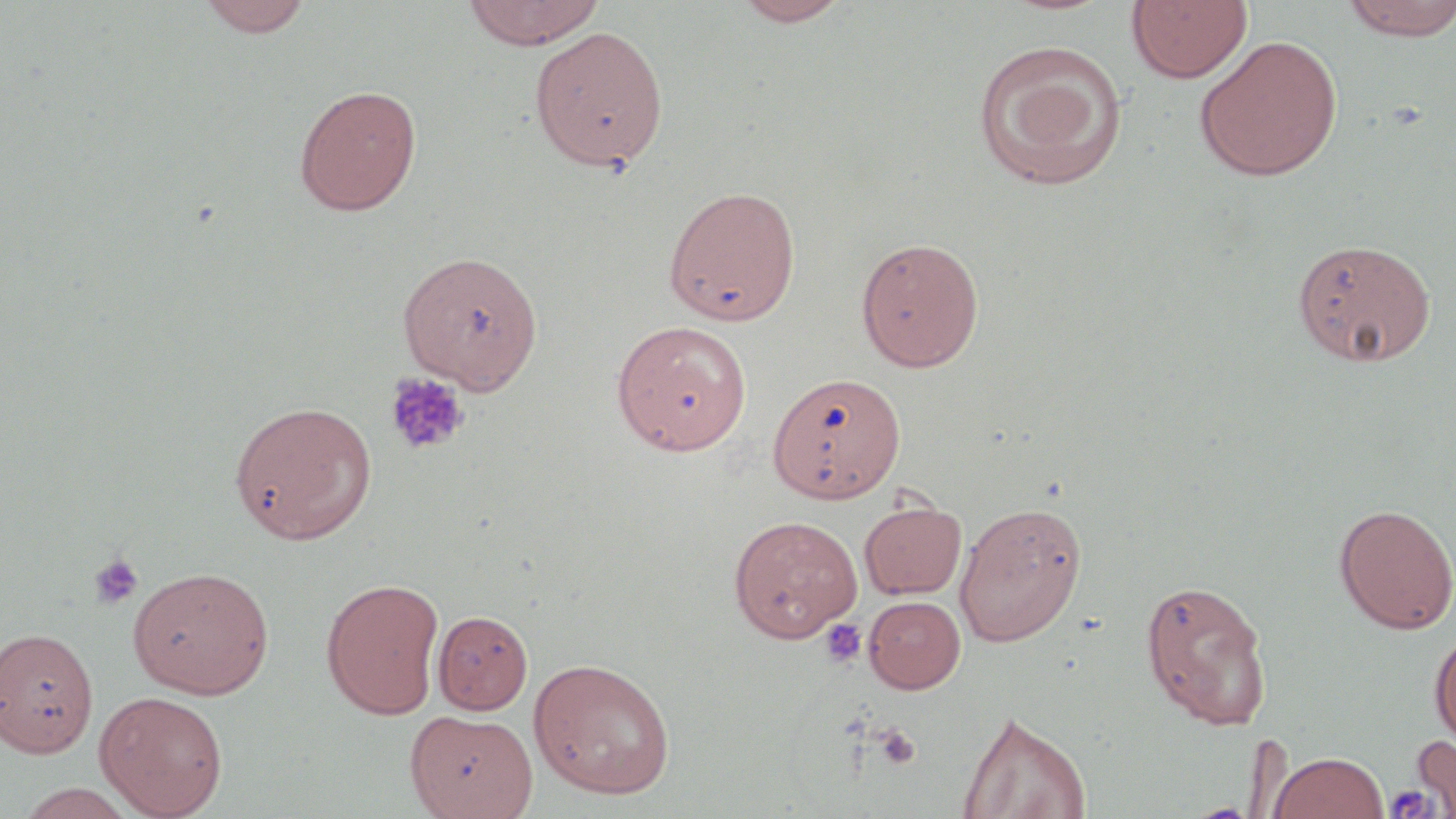
Summary:
  - Coordinate format: approximate bounding boxes as [x1, y1, x2, y2] in pixels
  - Uninfected red blood cell locations: [196, 0, 313, 37], [461, 0, 606, 49], [731, 0, 853, 26], [1125, 0, 1253, 84], [1340, 0, 1456, 41], [529, 26, 668, 172], [1194, 35, 1343, 182], [972, 39, 1129, 192], [293, 84, 422, 216], [663, 185, 801, 326], [855, 236, 985, 372], [1291, 237, 1437, 367], [397, 250, 544, 395], [610, 319, 752, 455], [767, 371, 905, 503], [229, 400, 377, 544], [859, 500, 967, 599], [954, 501, 1087, 647], [1334, 503, 1456, 634], [728, 515, 863, 643], [127, 565, 275, 699], [320, 577, 445, 719], [1139, 578, 1273, 730], [863, 595, 966, 693], [433, 609, 533, 714], [0, 626, 99, 758], [1429, 629, 1456, 752], [528, 657, 677, 800], [94, 690, 229, 818], [405, 709, 537, 819], [956, 710, 1092, 819], [1412, 730, 1456, 816], [1269, 751, 1388, 819], [14, 783, 144, 819]
  - Platelet locations: [384, 373, 470, 456], [88, 553, 145, 610], [820, 619, 867, 668], [875, 725, 921, 770], [1385, 784, 1436, 817]
  - Slide-level diagnosis: no evidence of blood parasites
  - Stain: May-Grünwald-Giemsa
  - Modality: optical microscopy
  - Magnification: 1000x
  - Preparation: thin blood smear
  - Field of view: single
  - Image size: 1456×819 pixels